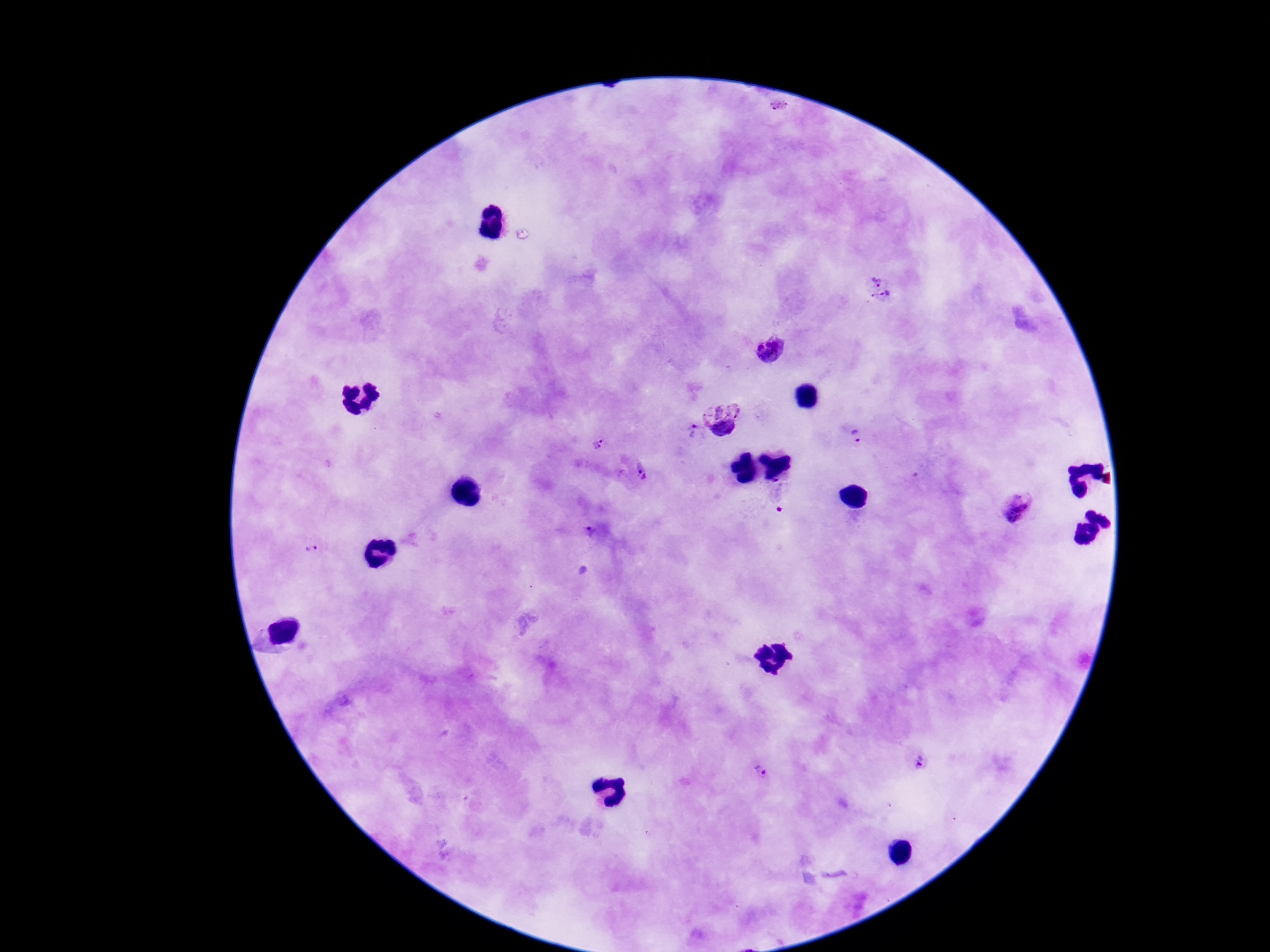

Approximate centers as {x, y} in pixels.
Summary:
  - Plasmodium parasite locations: {876, 277}, {886, 302}, {769, 348}, {724, 419}, {693, 433}, {857, 439}, {597, 445}, {642, 474}, {1017, 508}, {591, 531}, {310, 550}, {920, 760}, {759, 772}
  - Image size: 1270×952 pixels
  - Field of view: one from this slide
  - Patient malaria status: positive
  - Capture: smartphone camera through the microscope eyepiece
  - Preparation: thick blood smear
  - Stain: Giemsa
  - Magnification: 100x